State the blood parasite species.
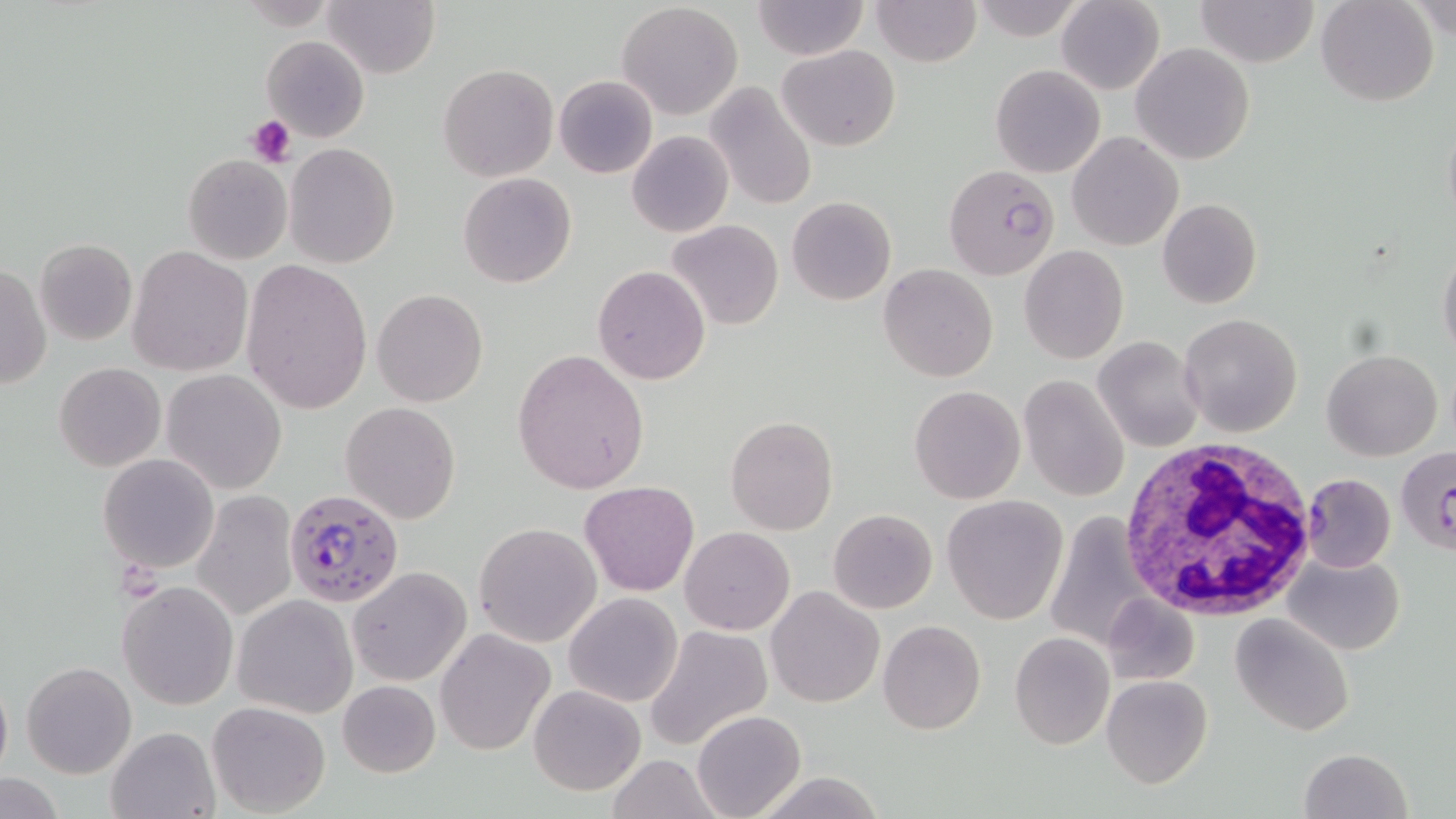

Plasmodium falciparum.

stain = May-Grünwald-Giemsa
image size = 1456×819 pixels
Plasmodium falciparum-infected red blood cell locations = approximate bounding boxes as named x1/y1/x2/y2 corners in pixels: (x1=945, y1=164, x2=1060, y2=280), (x1=1395, y1=447, x2=1455, y2=557), (x1=1299, y1=471, x2=1396, y2=574), (x1=283, y1=488, x2=405, y2=606)
platelet locations = approximate bounding boxes as named x1/y1/x2/y2 corners in pixels: (x1=247, y1=115, x2=297, y2=168)
uninfected red blood cell locations = approximate bounding boxes as named x1/y1/x2/y2 corners in pixels: (x1=321, y1=0, x2=439, y2=78), (x1=870, y1=0, x2=980, y2=67), (x1=1195, y1=0, x2=1319, y2=67), (x1=1314, y1=0, x2=1440, y2=107), (x1=751, y1=1, x2=868, y2=61), (x1=1056, y1=1, x2=1164, y2=94), (x1=617, y1=3, x2=744, y2=118), (x1=261, y1=36, x2=368, y2=142), (x1=1131, y1=43, x2=1256, y2=165), (x1=778, y1=44, x2=901, y2=150), (x1=439, y1=64, x2=559, y2=182), (x1=991, y1=64, x2=1106, y2=178), (x1=554, y1=75, x2=658, y2=179), (x1=704, y1=80, x2=816, y2=213), (x1=1441, y1=115, x2=1456, y2=231), (x1=627, y1=131, x2=733, y2=238), (x1=1067, y1=131, x2=1183, y2=251), (x1=285, y1=143, x2=399, y2=267), (x1=183, y1=154, x2=292, y2=264), (x1=459, y1=173, x2=577, y2=288), (x1=787, y1=195, x2=896, y2=305), (x1=1157, y1=197, x2=1263, y2=308), (x1=666, y1=219, x2=783, y2=332), (x1=34, y1=239, x2=137, y2=347), (x1=1438, y1=242, x2=1456, y2=362), (x1=1019, y1=245, x2=1129, y2=363), (x1=127, y1=246, x2=252, y2=376), (x1=241, y1=259, x2=372, y2=414), (x1=1, y1=263, x2=50, y2=391), (x1=593, y1=264, x2=709, y2=385), (x1=880, y1=264, x2=999, y2=383), (x1=372, y1=289, x2=488, y2=406), (x1=1179, y1=313, x2=1304, y2=437), (x1=1092, y1=336, x2=1205, y2=452), (x1=513, y1=348, x2=648, y2=492), (x1=1320, y1=349, x2=1443, y2=462), (x1=54, y1=362, x2=165, y2=472), (x1=162, y1=369, x2=286, y2=494), (x1=1019, y1=373, x2=1130, y2=502), (x1=908, y1=386, x2=1025, y2=503), (x1=340, y1=402, x2=462, y2=524), (x1=725, y1=417, x2=839, y2=536), (x1=99, y1=453, x2=218, y2=572), (x1=579, y1=480, x2=700, y2=597), (x1=191, y1=492, x2=299, y2=621), (x1=942, y1=494, x2=1069, y2=624), (x1=828, y1=508, x2=937, y2=613), (x1=1047, y1=516, x2=1158, y2=644), (x1=473, y1=523, x2=602, y2=647), (x1=679, y1=526, x2=796, y2=635), (x1=1281, y1=551, x2=1405, y2=656), (x1=348, y1=567, x2=472, y2=685), (x1=117, y1=580, x2=239, y2=710), (x1=766, y1=586, x2=885, y2=709), (x1=563, y1=592, x2=683, y2=708), (x1=233, y1=594, x2=357, y2=718), (x1=1102, y1=594, x2=1201, y2=686), (x1=1231, y1=612, x2=1357, y2=735), (x1=879, y1=620, x2=986, y2=735), (x1=643, y1=624, x2=772, y2=753), (x1=436, y1=628, x2=555, y2=755), (x1=1009, y1=631, x2=1115, y2=749), (x1=22, y1=662, x2=136, y2=779), (x1=0, y1=671, x2=11, y2=784), (x1=1100, y1=675, x2=1212, y2=788), (x1=336, y1=679, x2=441, y2=777), (x1=528, y1=684, x2=646, y2=796), (x1=206, y1=700, x2=331, y2=816), (x1=693, y1=710, x2=806, y2=819), (x1=106, y1=726, x2=220, y2=818), (x1=1299, y1=747, x2=1412, y2=819), (x1=603, y1=755, x2=728, y2=819), (x1=752, y1=773, x2=889, y2=817), (x1=0, y1=776, x2=66, y2=818)
white blood cell locations = approximate bounding boxes as named x1/y1/x2/y2 corners in pixels: (x1=1114, y1=439, x2=1316, y2=620)
magnification = 1000x
modality = light microscopy
field of view = one of a larger specimen
preparation = thin blood film